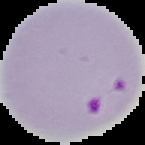 Image is 145×145 pixels. Result: malaria parasites identified. From a thin blood smear. Cell region segmented out of the field of view; the surrounding area is masked to black.